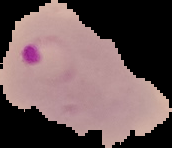
Summary:
  - Result: Plasmodium parasites identified
  - Image size: 172×148 pixels
  - Preparation: thin blood smear
  - Image type: segmented cell region on a black background